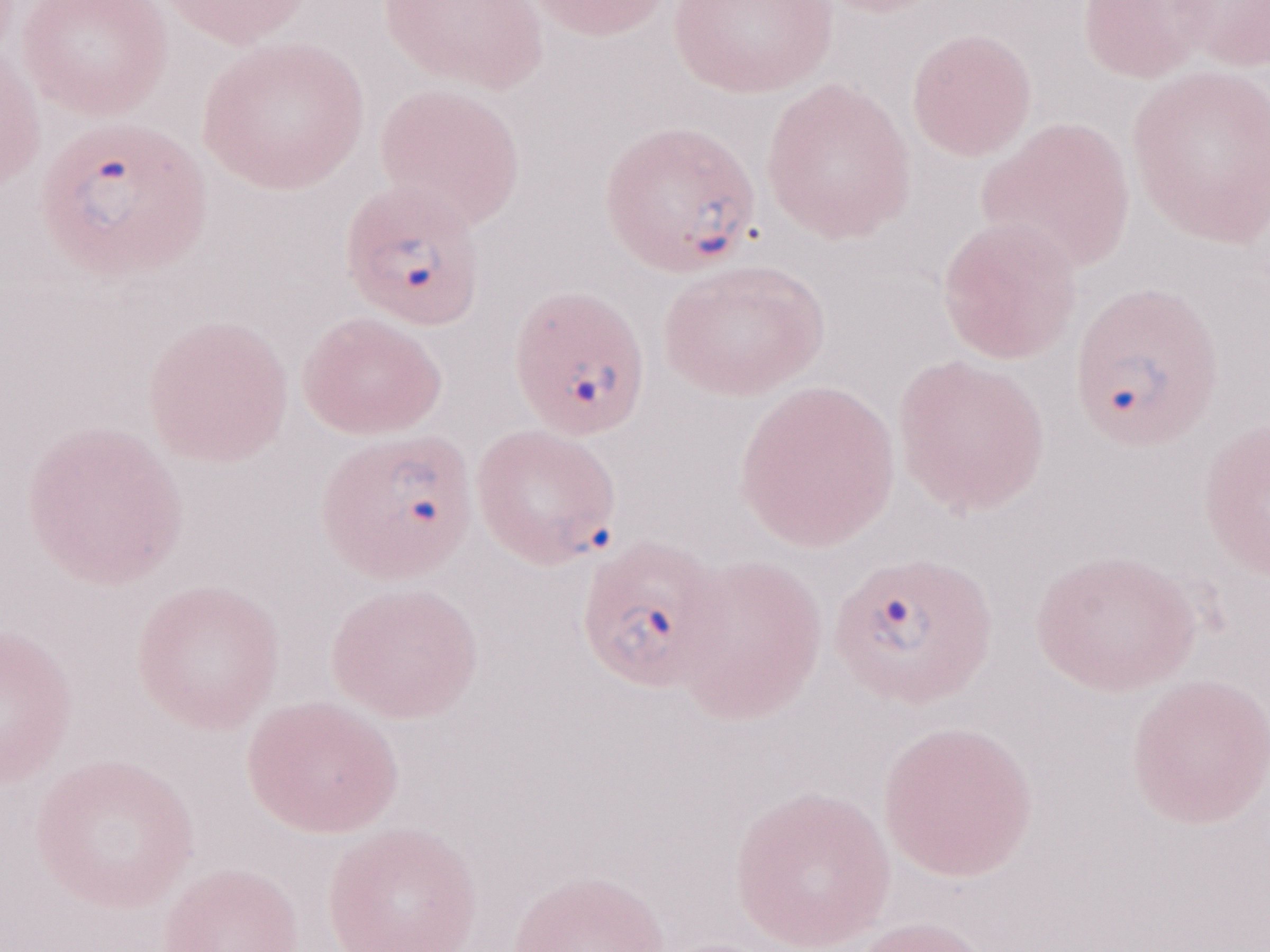
Single field of view. Patient-level malaria diagnosis: positive. Thin blood film. Olympus BX43 microscope, Olympus DP73 camera. Image is 1270×952 pixels. Magnification: 1,000x. May-Grünwald-Giemsa (MGG) stain.